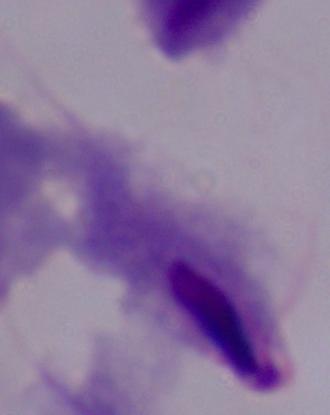
1000x magnification. A trichomonad is seen. Micrograph.